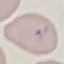 Malaria status: parasitized. Thin smear of blood. Cell patch, automatically extracted from a larger field of view and resized to 64 × 64 pixels. Photographed with a smartphone camera at the microscope eyepiece. Giemsa stain.